Describe the morphology of the erythrocytes.
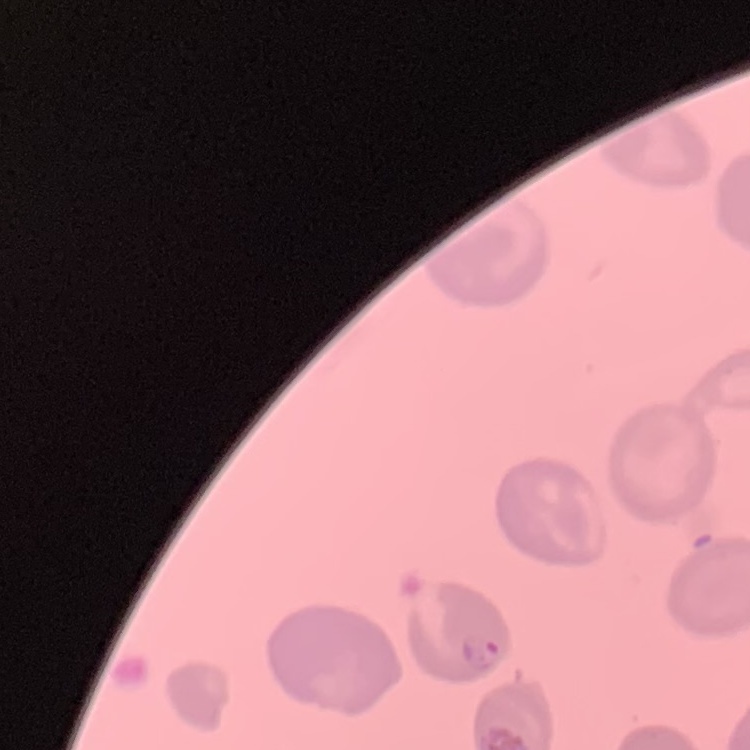
They show no rouleaux formation.

{
  "image_type": "square crop of a larger photomicrograph",
  "preparation": "thin blood smear",
  "stain": "Field's or Giemsa"
}